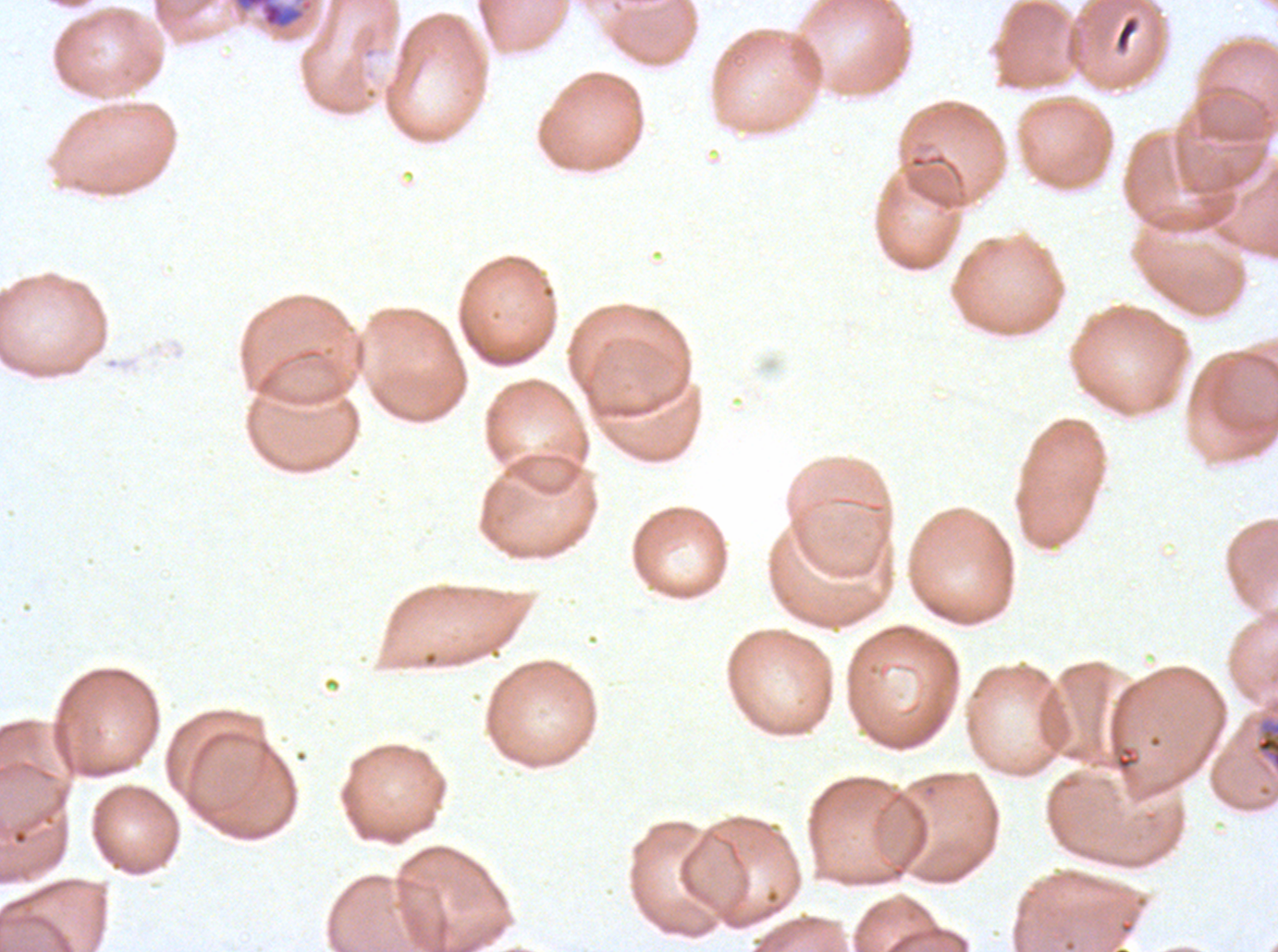

Approximate bounding boxes as [x1, y1, x2, y2] in pixels. Debris locations: [1114, 15, 1139, 53]. Late schizont locations: [1254, 716, 1277, 771]. Early schizont locations: [230, 0, 315, 33]. One sub-image of a larger composite. Image is 1278×952 pixels. Giemsa-stained preparation. Thin blood film. Ex-vivo Plasmodium falciparum culture from a patient in The Gambia, grown for 24 to 48 hours. Life-cycle stages observed: early schizont, late schizont.